Locate and identify every blood parasite.
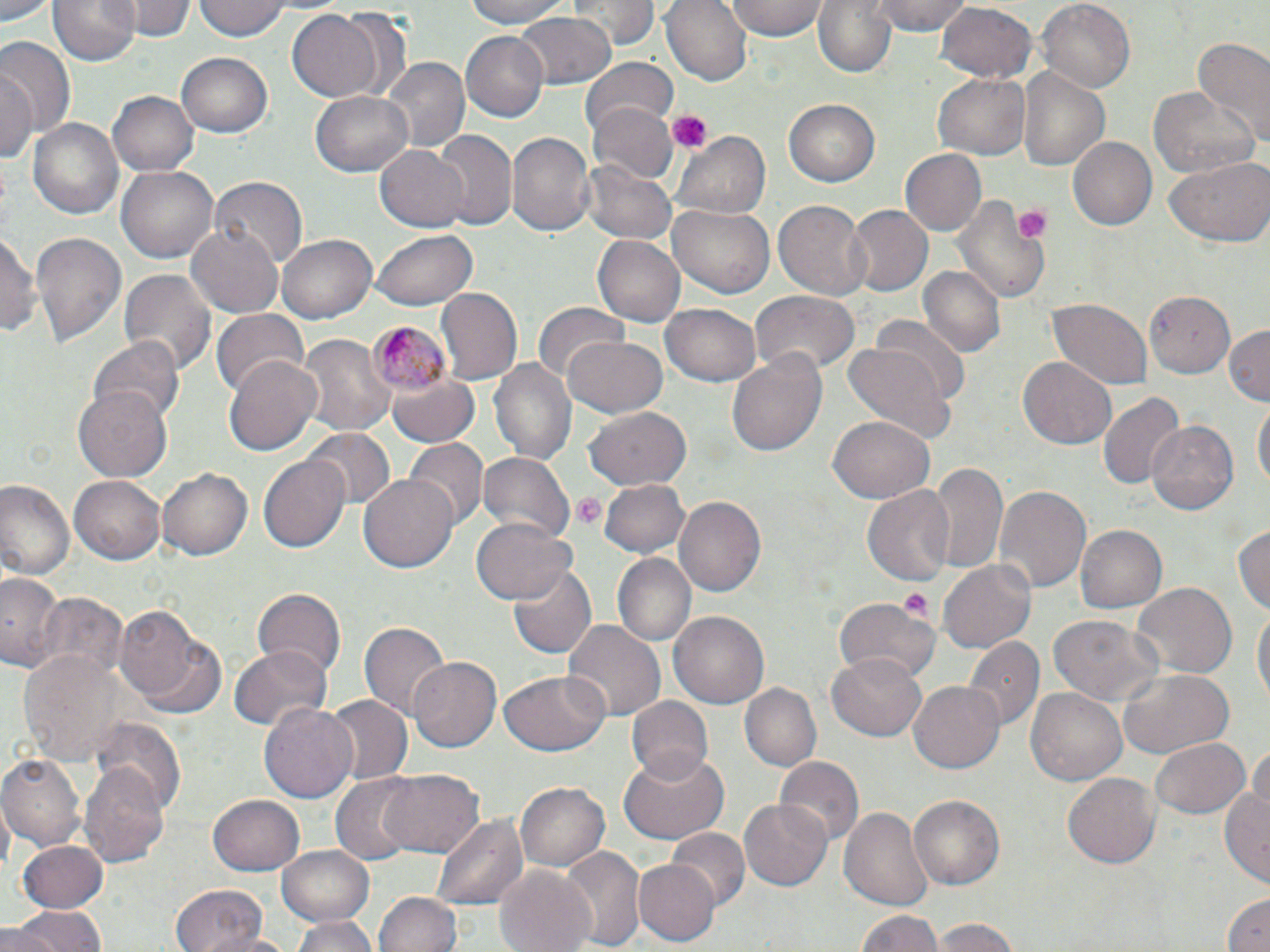

Approximate bounding boxes as named x1/y1/x2/y2 corners in pixels.
Plasmodium malariae-infected red blood cells: (x1=362, y1=323, x2=451, y2=395).
No Plasmodium falciparum, Plasmodium ovale, Plasmodium vivax, Babesia divergens, or Trypanosoma brucei observed.

Platelet locations: (x1=668, y1=111, x2=709, y2=154), (x1=1010, y1=203, x2=1050, y2=244), (x1=571, y1=491, x2=607, y2=529), (x1=896, y1=590, x2=935, y2=623). Uninfected red blood cell locations: (x1=0, y1=0, x2=57, y2=24), (x1=48, y1=0, x2=139, y2=65), (x1=129, y1=0, x2=191, y2=41), (x1=195, y1=0, x2=290, y2=40), (x1=458, y1=0, x2=580, y2=28), (x1=568, y1=0, x2=657, y2=49), (x1=661, y1=0, x2=752, y2=87), (x1=726, y1=0, x2=829, y2=40), (x1=812, y1=0, x2=896, y2=78), (x1=867, y1=0, x2=974, y2=35), (x1=1037, y1=0, x2=1134, y2=91), (x1=937, y1=2, x2=1038, y2=85), (x1=334, y1=7, x2=414, y2=105), (x1=288, y1=8, x2=384, y2=102), (x1=514, y1=9, x2=615, y2=89), (x1=460, y1=30, x2=551, y2=122), (x1=1191, y1=39, x2=1270, y2=146), (x1=0, y1=40, x2=73, y2=140), (x1=176, y1=52, x2=273, y2=139), (x1=580, y1=57, x2=678, y2=144), (x1=381, y1=58, x2=468, y2=154), (x1=0, y1=66, x2=37, y2=167), (x1=1018, y1=68, x2=1108, y2=173), (x1=932, y1=73, x2=1030, y2=160), (x1=1151, y1=84, x2=1258, y2=181), (x1=107, y1=89, x2=199, y2=177), (x1=311, y1=89, x2=415, y2=177), (x1=783, y1=96, x2=881, y2=185), (x1=590, y1=101, x2=676, y2=184), (x1=28, y1=116, x2=125, y2=221), (x1=673, y1=128, x2=770, y2=220), (x1=506, y1=131, x2=594, y2=240), (x1=432, y1=132, x2=516, y2=229), (x1=1069, y1=135, x2=1161, y2=230), (x1=374, y1=143, x2=468, y2=233), (x1=900, y1=148, x2=986, y2=237), (x1=1161, y1=157, x2=1270, y2=248), (x1=583, y1=160, x2=677, y2=244), (x1=117, y1=164, x2=218, y2=264), (x1=211, y1=175, x2=307, y2=271), (x1=951, y1=197, x2=1052, y2=303), (x1=772, y1=200, x2=870, y2=299), (x1=667, y1=202, x2=774, y2=299), (x1=844, y1=204, x2=932, y2=296), (x1=185, y1=220, x2=281, y2=317), (x1=1, y1=228, x2=40, y2=340), (x1=372, y1=229, x2=478, y2=310), (x1=30, y1=231, x2=125, y2=348), (x1=277, y1=234, x2=376, y2=324), (x1=593, y1=234, x2=685, y2=327), (x1=918, y1=266, x2=1005, y2=358), (x1=119, y1=268, x2=216, y2=378), (x1=437, y1=288, x2=522, y2=384), (x1=1144, y1=289, x2=1236, y2=378), (x1=750, y1=291, x2=859, y2=376), (x1=1046, y1=298, x2=1154, y2=388), (x1=532, y1=302, x2=628, y2=388), (x1=662, y1=304, x2=760, y2=387), (x1=212, y1=311, x2=309, y2=399), (x1=873, y1=316, x2=970, y2=404), (x1=1225, y1=324, x2=1269, y2=404), (x1=295, y1=329, x2=394, y2=437), (x1=560, y1=334, x2=666, y2=418), (x1=88, y1=335, x2=184, y2=421), (x1=845, y1=343, x2=951, y2=441), (x1=727, y1=353, x2=826, y2=456), (x1=226, y1=354, x2=324, y2=457), (x1=1017, y1=357, x2=1117, y2=449), (x1=488, y1=358, x2=577, y2=466), (x1=386, y1=366, x2=481, y2=448), (x1=74, y1=385, x2=172, y2=481), (x1=1097, y1=393, x2=1184, y2=493), (x1=1253, y1=400, x2=1269, y2=492), (x1=585, y1=405, x2=694, y2=490), (x1=829, y1=413, x2=932, y2=501), (x1=1145, y1=418, x2=1242, y2=517), (x1=305, y1=426, x2=396, y2=510), (x1=406, y1=439, x2=486, y2=525), (x1=258, y1=449, x2=351, y2=552), (x1=479, y1=452, x2=573, y2=542), (x1=926, y1=462, x2=1009, y2=578), (x1=158, y1=466, x2=254, y2=562), (x1=71, y1=474, x2=165, y2=563), (x1=359, y1=475, x2=458, y2=573), (x1=598, y1=477, x2=690, y2=559), (x1=0, y1=479, x2=75, y2=580), (x1=991, y1=481, x2=1090, y2=591), (x1=862, y1=484, x2=953, y2=586), (x1=674, y1=495, x2=767, y2=599), (x1=474, y1=515, x2=574, y2=605), (x1=1234, y1=520, x2=1269, y2=619), (x1=1074, y1=524, x2=1166, y2=613), (x1=614, y1=553, x2=695, y2=648), (x1=939, y1=557, x2=1036, y2=653), (x1=507, y1=562, x2=596, y2=660), (x1=0, y1=572, x2=66, y2=672), (x1=1130, y1=583, x2=1235, y2=681), (x1=251, y1=587, x2=344, y2=674), (x1=38, y1=591, x2=127, y2=681), (x1=834, y1=596, x2=938, y2=686), (x1=1252, y1=602, x2=1269, y2=711), (x1=117, y1=604, x2=213, y2=711), (x1=671, y1=611, x2=769, y2=709), (x1=1046, y1=616, x2=1165, y2=707), (x1=360, y1=620, x2=450, y2=720), (x1=561, y1=620, x2=665, y2=722), (x1=965, y1=636, x2=1042, y2=729), (x1=229, y1=643, x2=330, y2=733), (x1=17, y1=651, x2=127, y2=766), (x1=827, y1=654, x2=928, y2=742), (x1=406, y1=656, x2=501, y2=753), (x1=1119, y1=668, x2=1231, y2=756), (x1=500, y1=671, x2=608, y2=757), (x1=909, y1=681, x2=1005, y2=774), (x1=741, y1=683, x2=822, y2=772), (x1=1026, y1=688, x2=1128, y2=788), (x1=322, y1=695, x2=411, y2=785), (x1=627, y1=697, x2=714, y2=783), (x1=260, y1=701, x2=359, y2=804), (x1=90, y1=718, x2=187, y2=814), (x1=1149, y1=737, x2=1248, y2=818), (x1=1249, y1=742, x2=1269, y2=821), (x1=618, y1=750, x2=730, y2=845), (x1=0, y1=754, x2=85, y2=852), (x1=774, y1=756, x2=862, y2=850), (x1=79, y1=762, x2=172, y2=868), (x1=379, y1=768, x2=483, y2=858), (x1=1062, y1=771, x2=1161, y2=869), (x1=330, y1=776, x2=421, y2=865), (x1=1221, y1=778, x2=1270, y2=889), (x1=516, y1=779, x2=610, y2=870), (x1=908, y1=793, x2=1005, y2=887), (x1=208, y1=794, x2=305, y2=877), (x1=740, y1=800, x2=832, y2=891), (x1=839, y1=803, x2=935, y2=911), (x1=434, y1=814, x2=527, y2=911), (x1=666, y1=828, x2=750, y2=913), (x1=18, y1=839, x2=108, y2=912), (x1=276, y1=844, x2=375, y2=925), (x1=560, y1=845, x2=644, y2=949), (x1=633, y1=859, x2=719, y2=945), (x1=494, y1=864, x2=597, y2=952), (x1=169, y1=885, x2=269, y2=952), (x1=375, y1=891, x2=464, y2=952), (x1=1221, y1=892, x2=1269, y2=951), (x1=7, y1=908, x2=109, y2=952), (x1=854, y1=908, x2=946, y2=952), (x1=292, y1=915, x2=378, y2=952), (x1=931, y1=918, x2=1026, y2=952), (x1=0, y1=926, x2=64, y2=952), (x1=203, y1=928, x2=297, y2=952). Slide-level diagnosis: Plasmodium malariae. Image is 1270×952 pixels. May-Grünwald-Giemsa-stained preparation. One field of a larger specimen. Thin blood smear. 1000x magnification. Light microscopy.